Describe the morphology of the red blood cells.
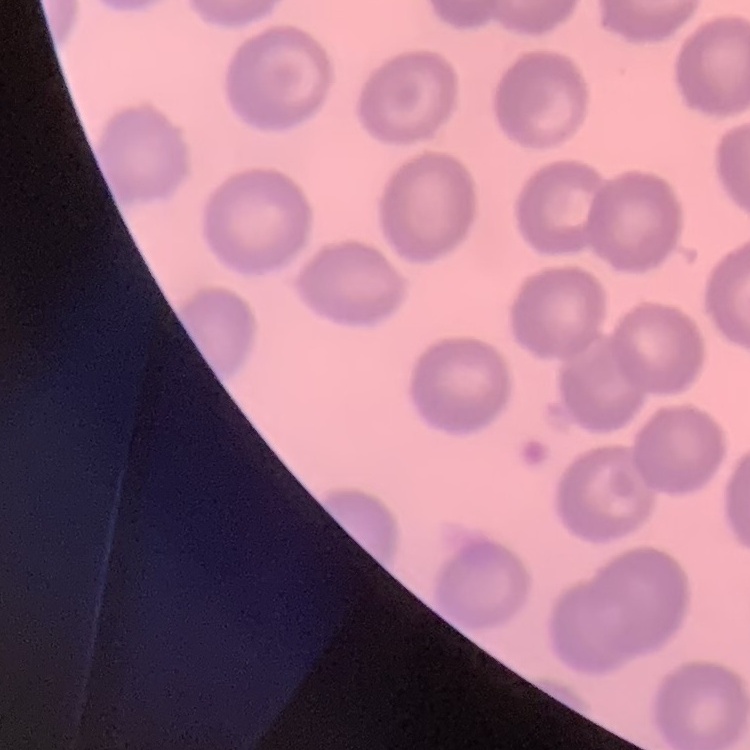
They show no rouleaux formation.

Field's or Giemsa stain. Thin blood smear. Square crop of a larger photomicrograph.